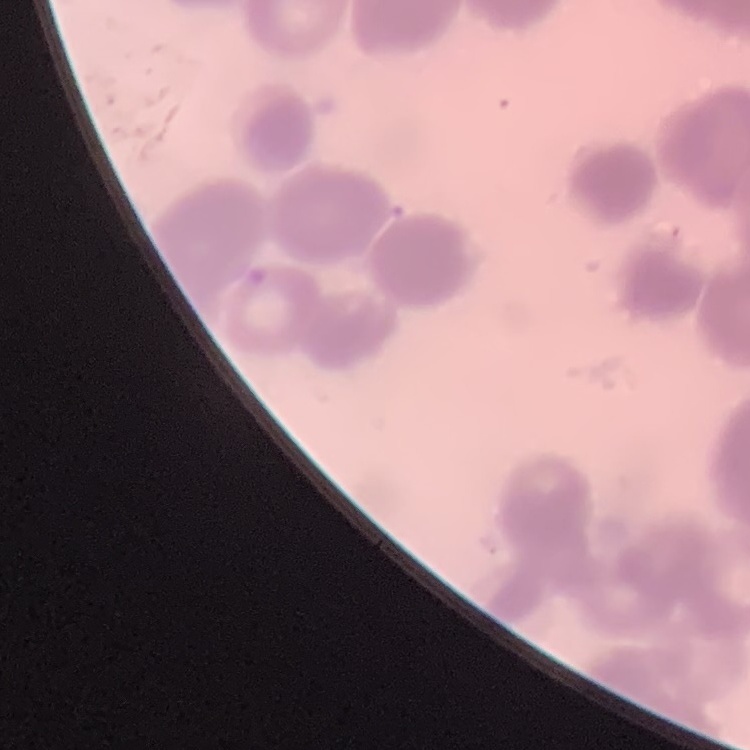
red blood cell morphology = rouleaux formation
stain = Field's or Giemsa
image type = one tile cut from a larger photomicrograph
preparation = thin blood smear